Assess this cell for malaria.
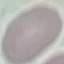

Uninfected.

{
  "stain": "Giemsa",
  "preparation": "thin blood smear",
  "capture": "smartphone camera at the microscope eyepiece",
  "image_type": "cell patch, automatically extracted from a larger field of view and resized to 64 × 64 pixels"
}